Locate and identify every blood parasite.
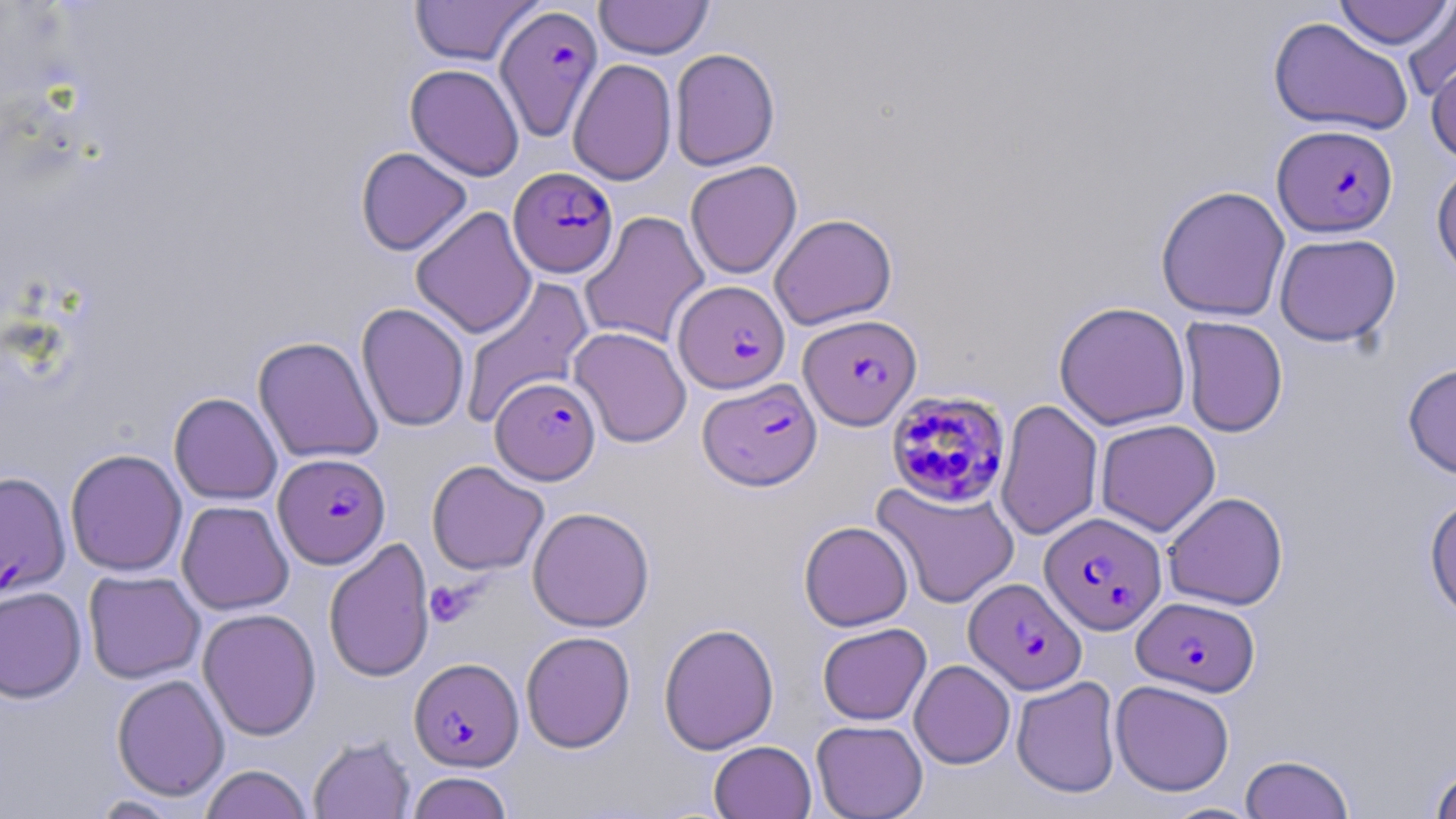

Approximate bounding boxes as (x1,y1)-(x2,y2) corner pairs in pixels.
Plasmodium falciparum-infected red blood cells: (494,4)-(603,142), (1273,124)-(1398,237), (508,167)-(618,278), (674,280)-(790,394), (799,313)-(921,430), (491,377)-(600,484), (698,377)-(822,491), (886,389)-(1012,508), (273,453)-(391,569), (0,471)-(70,598), (1039,512)-(1167,634), (964,578)-(1086,694), (1133,596)-(1259,696), (409,657)-(523,771).
No Plasmodium ovale, Plasmodium malariae, Plasmodium vivax, Babesia divergens, or Trypanosoma brucei observed.

Summary:
  - Platelet locations: (424,580)-(478,627)
  - Uninfected red blood cell locations: (1333,0)-(1454,50), (409,1)-(543,67), (594,1)-(713,59), (1402,2)-(1456,102), (1268,17)-(1414,137), (669,48)-(780,170), (1426,54)-(1456,163), (568,58)-(677,186), (356,147)-(472,256), (684,160)-(802,279), (1431,161)-(1456,283), (1155,185)-(1291,321), (410,206)-(537,339), (580,211)-(710,348), (769,213)-(897,330), (1274,232)-(1401,347), (460,276)-(594,427), (1053,301)-(1191,430), (356,303)-(470,432), (1179,316)-(1288,438), (569,326)-(691,448), (253,336)-(383,464), (1402,360)-(1456,480), (169,392)-(282,505), (996,399)-(1103,540), (1095,419)-(1220,536), (65,449)-(187,576), (426,460)-(549,576), (871,480)-(1020,610), (1163,492)-(1288,611), (1424,492)-(1456,623), (176,500)-(294,615), (527,506)-(655,632), (798,520)-(913,631), (324,537)-(435,683), (83,570)-(205,683), (0,586)-(86,703), (197,608)-(322,740), (658,622)-(779,755), (817,622)-(931,725), (520,631)-(636,752), (909,660)-(1015,769), (111,674)-(230,801), (1011,676)-(1122,798), (1110,680)-(1234,796), (811,719)-(928,818), (308,736)-(415,818), (709,740)-(816,819), (1240,754)-(1354,818), (1429,763)-(1456,819), (199,764)-(313,819), (405,771)-(514,819), (88,795)-(186,818), (1161,802)-(1262,819)
  - Slide-level diagnosis: Plasmodium falciparum
  - Field of view: one of a larger specimen
  - Image size: 1456×819 pixels
  - Stain: May-Grünwald-Giemsa
  - Modality: optical microscopy
  - Magnification: 1000x
  - Preparation: thin blood film